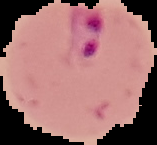

image size = 157×145 pixels
result = Plasmodium parasites identified
image type = segmented cell region with the area outside set to black
preparation = thin blood smear